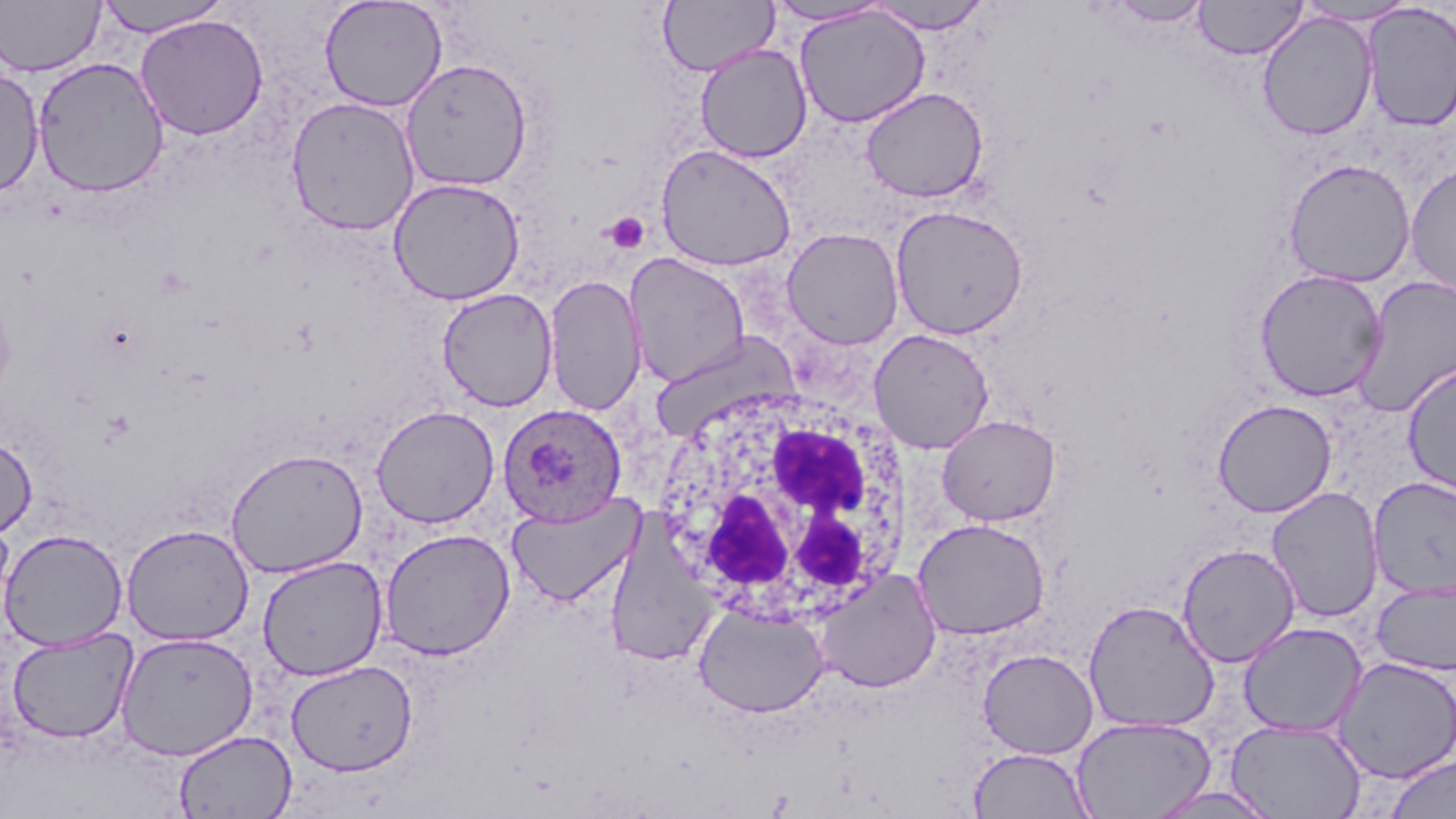

Approximate bounding boxes as named x1/y1/x2/y2 corners in pixels. White blood cell locations: (x1=662, y1=385, x2=916, y2=629). Platelet locations: (x1=605, y1=212, x2=650, y2=254). Plasmodium ovale-infected red blood cell locations: (x1=498, y1=403, x2=627, y2=527). Uninfected red blood cell locations: (x1=320, y1=0, x2=448, y2=112), (x1=767, y1=0, x2=894, y2=27), (x1=1104, y1=0, x2=1214, y2=27), (x1=1194, y1=0, x2=1307, y2=60), (x1=0, y1=1, x2=104, y2=76), (x1=93, y1=1, x2=233, y2=36), (x1=657, y1=1, x2=778, y2=77), (x1=864, y1=1, x2=994, y2=34), (x1=1296, y1=1, x2=1417, y2=26), (x1=1361, y1=2, x2=1456, y2=132), (x1=794, y1=5, x2=931, y2=128), (x1=1257, y1=11, x2=1378, y2=141), (x1=134, y1=14, x2=270, y2=140), (x1=695, y1=43, x2=813, y2=163), (x1=32, y1=56, x2=169, y2=198), (x1=400, y1=58, x2=534, y2=192), (x1=0, y1=66, x2=44, y2=198), (x1=860, y1=86, x2=989, y2=203), (x1=285, y1=96, x2=421, y2=237), (x1=655, y1=143, x2=797, y2=271), (x1=1283, y1=158, x2=1417, y2=288), (x1=1404, y1=162, x2=1456, y2=298), (x1=387, y1=176, x2=526, y2=305), (x1=890, y1=204, x2=1029, y2=339), (x1=781, y1=226, x2=905, y2=349), (x1=625, y1=253, x2=750, y2=387), (x1=1254, y1=268, x2=1388, y2=402), (x1=543, y1=273, x2=645, y2=416), (x1=1353, y1=274, x2=1456, y2=418), (x1=437, y1=287, x2=558, y2=411), (x1=868, y1=328, x2=995, y2=454), (x1=648, y1=330, x2=800, y2=443), (x1=1401, y1=360, x2=1456, y2=499), (x1=1212, y1=399, x2=1337, y2=517), (x1=370, y1=404, x2=500, y2=528), (x1=937, y1=414, x2=1061, y2=526), (x1=0, y1=436, x2=37, y2=539), (x1=225, y1=447, x2=368, y2=579), (x1=1368, y1=477, x2=1456, y2=600), (x1=1266, y1=486, x2=1384, y2=622), (x1=506, y1=490, x2=645, y2=608), (x1=0, y1=514, x2=16, y2=639), (x1=912, y1=517, x2=1052, y2=641), (x1=604, y1=522, x2=718, y2=668), (x1=120, y1=523, x2=255, y2=646), (x1=379, y1=527, x2=516, y2=661), (x1=0, y1=528, x2=128, y2=651), (x1=1176, y1=543, x2=1300, y2=668), (x1=257, y1=555, x2=389, y2=681), (x1=813, y1=570, x2=942, y2=693), (x1=1370, y1=580, x2=1456, y2=676), (x1=1082, y1=599, x2=1220, y2=734), (x1=694, y1=602, x2=829, y2=718), (x1=1238, y1=622, x2=1367, y2=738), (x1=6, y1=627, x2=138, y2=745), (x1=115, y1=631, x2=258, y2=761), (x1=977, y1=649, x2=1099, y2=759), (x1=1332, y1=658, x2=1456, y2=783), (x1=286, y1=659, x2=418, y2=776), (x1=1071, y1=716, x2=1216, y2=819), (x1=1225, y1=719, x2=1367, y2=818), (x1=174, y1=730, x2=297, y2=819), (x1=968, y1=747, x2=1095, y2=819), (x1=1384, y1=755, x2=1455, y2=819), (x1=1143, y1=787, x2=1281, y2=818). Slide-level diagnosis: Plasmodium ovale. Image is 1456×819 pixels. Captured at 1000x magnification. Thin blood smear. One field of a larger specimen. May-Grünwald-Giemsa stain. Optical microscopy.